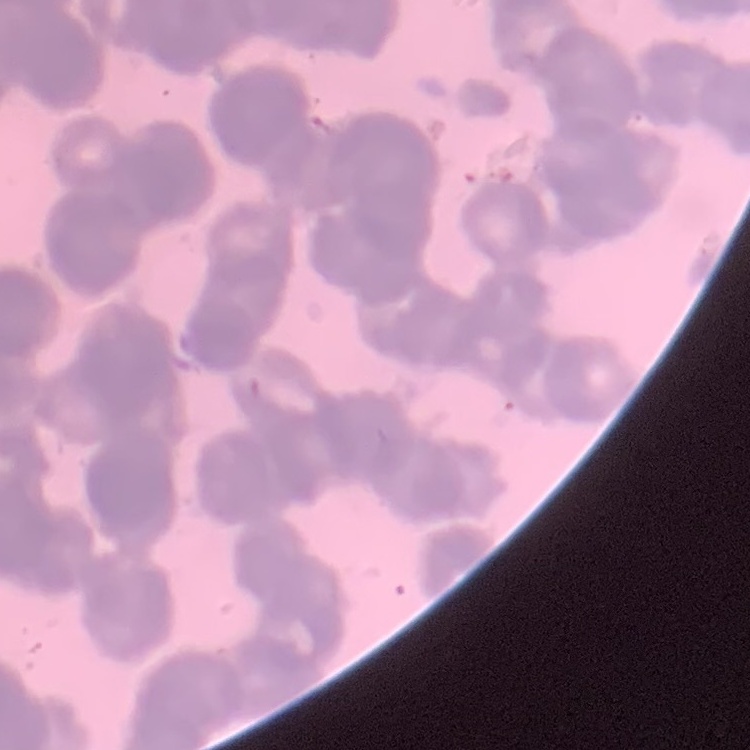
Summary:
  - Erythrocyte morphology: rouleaux formation
  - Preparation: thin blood smear
  - Stain: Field's or Giemsa
  - Image type: one tile cut from a larger photomicrograph